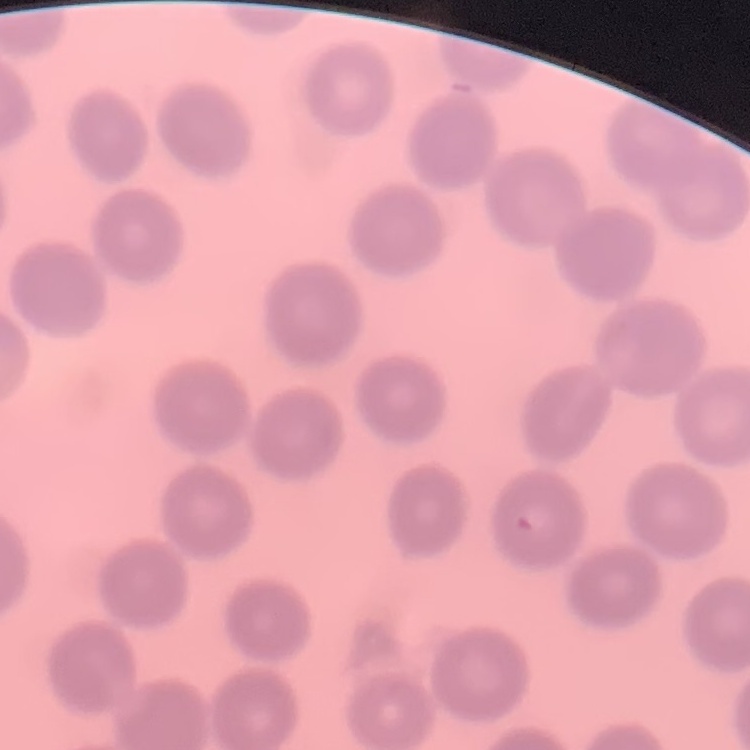
red_blood_cell_morphology: no rouleaux formation
image_type: one tile cut from a larger photomicrograph
stain: Field's or Giemsa
preparation: thin blood smear